Locate and identify every blood parasite.
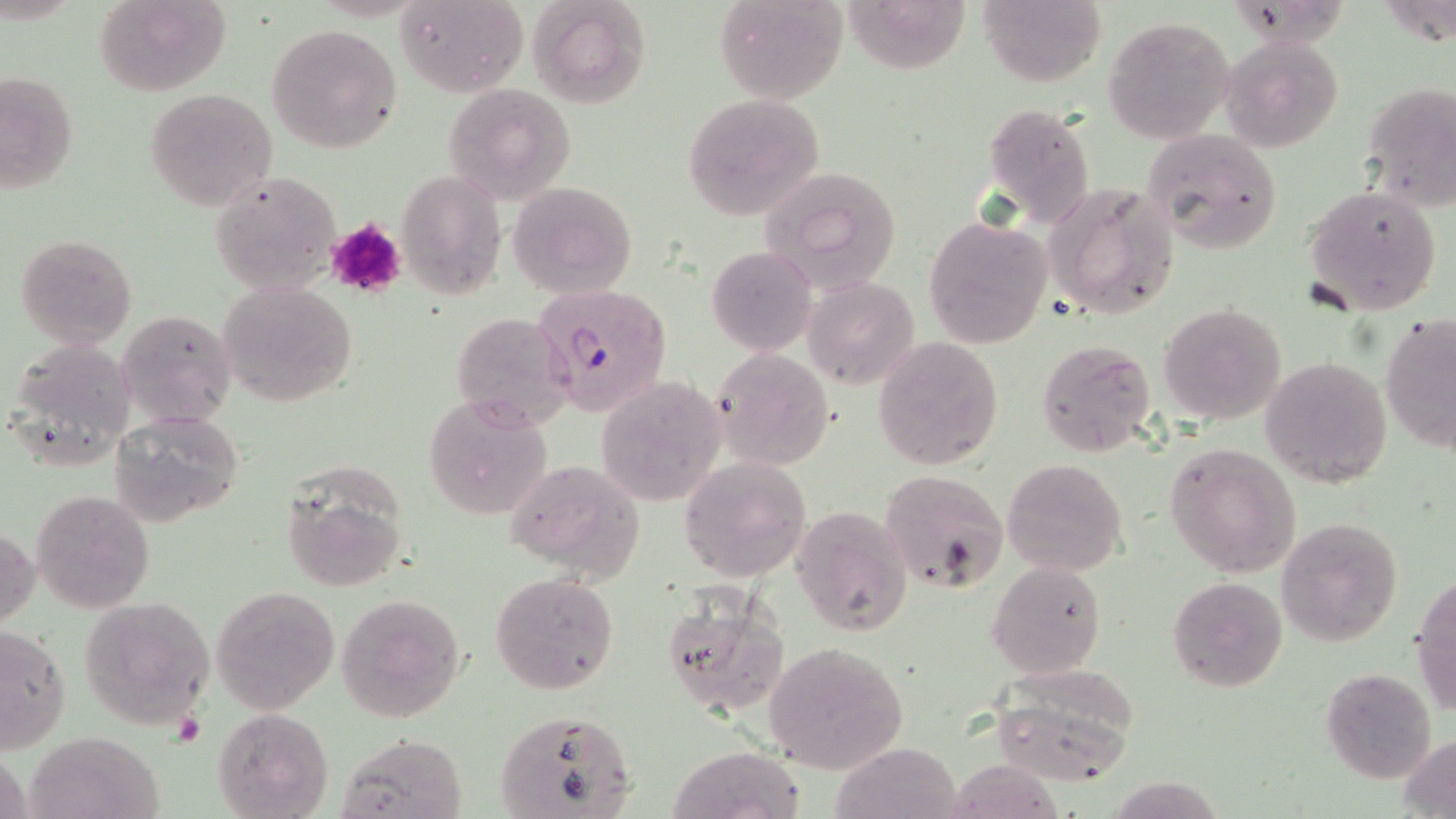

Approximate bounding boxes as named x1/y1/x2/y2 corners in pixels.
Plasmodium falciparum-infected red blood cells: (x1=534, y1=283, x2=673, y2=417).
No Plasmodium ovale, Plasmodium malariae, Plasmodium vivax, Babesia divergens, or Trypanosoma brucei observed.

slide-level diagnosis = Plasmodium falciparum
magnification = 1000x
field of view = one of a larger specimen
platelet locations = approximate bounding boxes as named x1/y1/x2/y2 corners in pixels: (x1=325, y1=216, x2=408, y2=299)
modality = light microscopy
uninfected red blood cell locations = approximate bounding boxes as named x1/y1/x2/y2 corners in pixels: (x1=93, y1=0, x2=230, y2=95), (x1=397, y1=0, x2=528, y2=96), (x1=528, y1=0, x2=651, y2=109), (x1=715, y1=0, x2=848, y2=105), (x1=974, y1=0, x2=1106, y2=86), (x1=1380, y1=0, x2=1454, y2=50), (x1=843, y1=4, x2=968, y2=80), (x1=1102, y1=16, x2=1235, y2=143), (x1=267, y1=23, x2=402, y2=154), (x1=1222, y1=35, x2=1345, y2=152), (x1=2, y1=68, x2=79, y2=196), (x1=1359, y1=80, x2=1456, y2=211), (x1=442, y1=81, x2=576, y2=206), (x1=143, y1=88, x2=278, y2=210), (x1=682, y1=94, x2=824, y2=220), (x1=982, y1=102, x2=1097, y2=228), (x1=1141, y1=126, x2=1283, y2=256), (x1=758, y1=166, x2=903, y2=296), (x1=396, y1=170, x2=505, y2=300), (x1=208, y1=171, x2=343, y2=297), (x1=506, y1=180, x2=637, y2=297), (x1=1046, y1=181, x2=1180, y2=318), (x1=1301, y1=185, x2=1442, y2=315), (x1=924, y1=214, x2=1053, y2=350), (x1=15, y1=233, x2=138, y2=350), (x1=706, y1=245, x2=817, y2=356), (x1=802, y1=275, x2=919, y2=389), (x1=217, y1=280, x2=357, y2=406), (x1=1159, y1=303, x2=1287, y2=425), (x1=116, y1=310, x2=236, y2=428), (x1=451, y1=310, x2=574, y2=430), (x1=1381, y1=314, x2=1456, y2=454), (x1=872, y1=336, x2=1003, y2=470), (x1=7, y1=339, x2=136, y2=469), (x1=1037, y1=339, x2=1158, y2=456), (x1=712, y1=347, x2=836, y2=470), (x1=1261, y1=354, x2=1392, y2=488), (x1=597, y1=377, x2=726, y2=507), (x1=424, y1=393, x2=553, y2=520), (x1=107, y1=409, x2=245, y2=527), (x1=1164, y1=442, x2=1303, y2=577), (x1=679, y1=456, x2=812, y2=581), (x1=503, y1=457, x2=646, y2=583), (x1=1002, y1=457, x2=1127, y2=576), (x1=278, y1=463, x2=410, y2=592), (x1=877, y1=469, x2=1010, y2=594), (x1=31, y1=489, x2=155, y2=614), (x1=792, y1=504, x2=914, y2=637), (x1=1275, y1=517, x2=1404, y2=646), (x1=1, y1=525, x2=40, y2=633), (x1=987, y1=559, x2=1107, y2=679), (x1=1413, y1=569, x2=1456, y2=720), (x1=489, y1=572, x2=620, y2=694), (x1=1167, y1=575, x2=1288, y2=693), (x1=212, y1=585, x2=340, y2=714), (x1=658, y1=588, x2=791, y2=718), (x1=336, y1=591, x2=466, y2=724), (x1=81, y1=597, x2=216, y2=728), (x1=1, y1=624, x2=71, y2=752), (x1=762, y1=640, x2=909, y2=775), (x1=1320, y1=667, x2=1438, y2=784), (x1=991, y1=669, x2=1141, y2=784), (x1=492, y1=705, x2=639, y2=818), (x1=213, y1=708, x2=332, y2=819), (x1=26, y1=731, x2=166, y2=819), (x1=339, y1=734, x2=468, y2=819), (x1=1397, y1=734, x2=1456, y2=818), (x1=832, y1=742, x2=960, y2=818), (x1=668, y1=744, x2=806, y2=819), (x1=1, y1=747, x2=31, y2=819), (x1=949, y1=752, x2=1068, y2=819)
image size = 1456×819 pixels
preparation = thin blood smear
stain = May-Grünwald-Giemsa